Give the extent of all Plasmodium ovale-infected red blood cells.
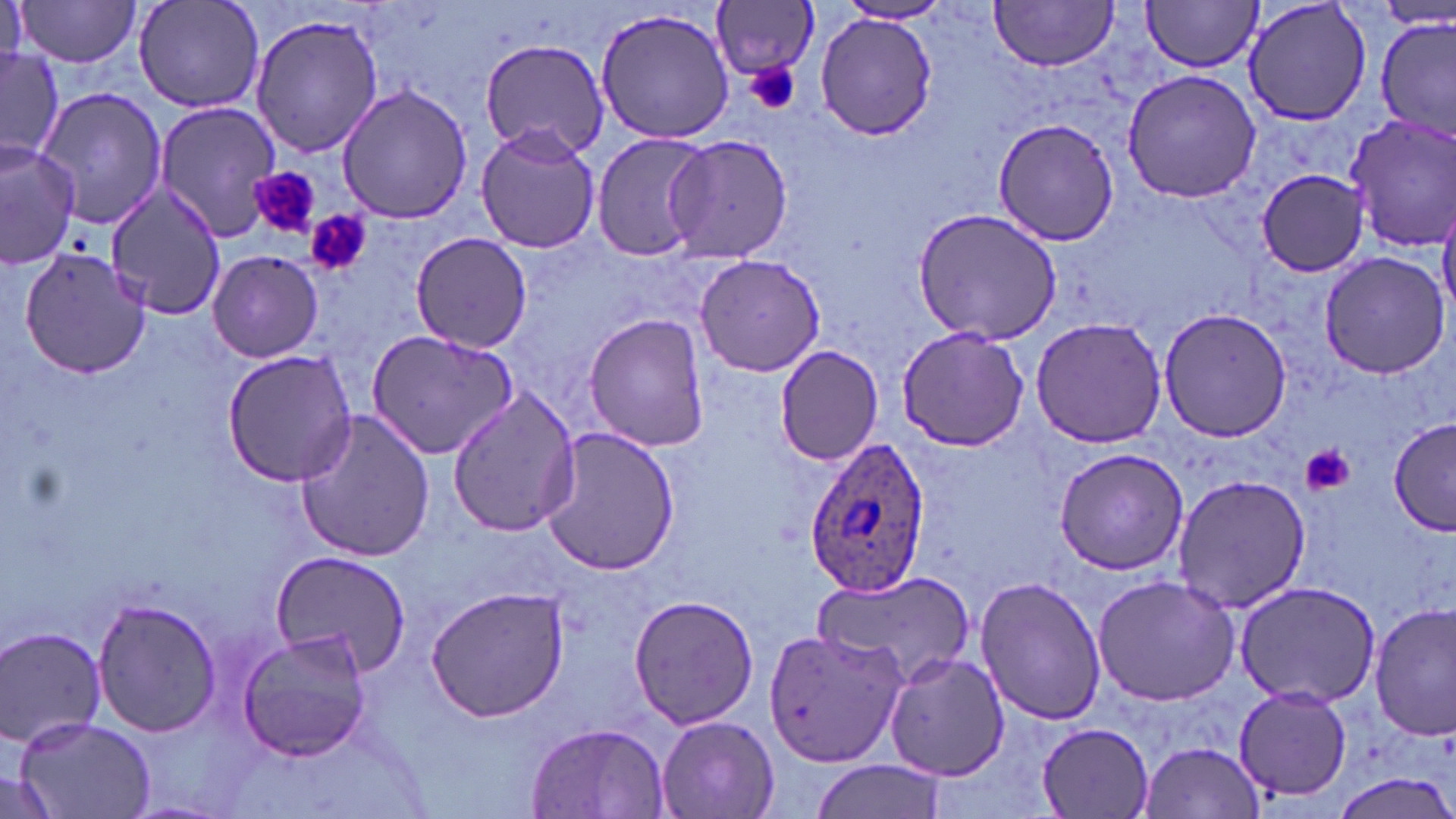
Approximate bounding boxes as (x1,y1)-(x2,y2) corner pairs in pixels.
Plasmodium ovale-infected red blood cells: (800,437)-(932,596).

Platelet locations: (745,63)-(801,115), (251,167)-(321,240), (306,210)-(370,276), (1303,444)-(1355,496). Uninfected red blood cell locations: (15,0)-(146,67), (134,0)-(265,114), (1143,0)-(1263,74), (1242,0)-(1371,127), (989,1)-(1119,72), (835,2)-(956,26), (711,3)-(821,83), (594,7)-(738,144), (814,13)-(938,139), (249,14)-(383,162), (1377,16)-(1455,139), (479,37)-(610,161), (0,46)-(62,167), (1121,68)-(1259,204), (336,84)-(476,223), (32,87)-(171,230), (153,99)-(282,241), (1342,112)-(1456,253), (992,117)-(1121,246), (474,124)-(601,253), (589,130)-(711,263), (664,133)-(795,263), (0,140)-(81,268), (1258,168)-(1372,276), (103,186)-(230,319), (1438,191)-(1456,317), (914,208)-(1062,345), (409,231)-(533,353), (17,246)-(152,377), (207,250)-(324,363), (1318,250)-(1450,379), (693,252)-(825,377), (1158,308)-(1291,445), (583,313)-(711,452), (1031,316)-(1168,448), (896,324)-(1029,452), (364,329)-(520,461), (773,345)-(883,465), (221,348)-(357,488), (447,387)-(582,538), (294,411)-(437,564), (1389,416)-(1456,534), (540,426)-(681,576), (1052,446)-(1192,575), (1170,473)-(1313,614), (268,549)-(413,674), (812,574)-(974,682), (1093,574)-(1242,707), (975,575)-(1106,726), (1232,579)-(1383,709), (424,586)-(571,722), (628,594)-(761,730), (94,599)-(222,734), (1370,604)-(1454,742), (0,625)-(108,750), (237,628)-(374,762), (762,629)-(906,768), (883,651)-(1009,782), (1233,687)-(1354,802), (656,713)-(779,819), (14,714)-(156,817), (1037,722)-(1157,818), (525,723)-(670,818), (1138,741)-(1265,818), (809,760)-(946,819), (0,769)-(57,817), (1336,774)-(1453,819). Slide-level diagnosis: Plasmodium ovale. Thin blood smear. 1000x magnification. One field of a larger specimen. Image is 1456×819 pixels. May-Grünwald-Giemsa-stained preparation. Light microscopy.